Assess the morphology of the erythrocytes.
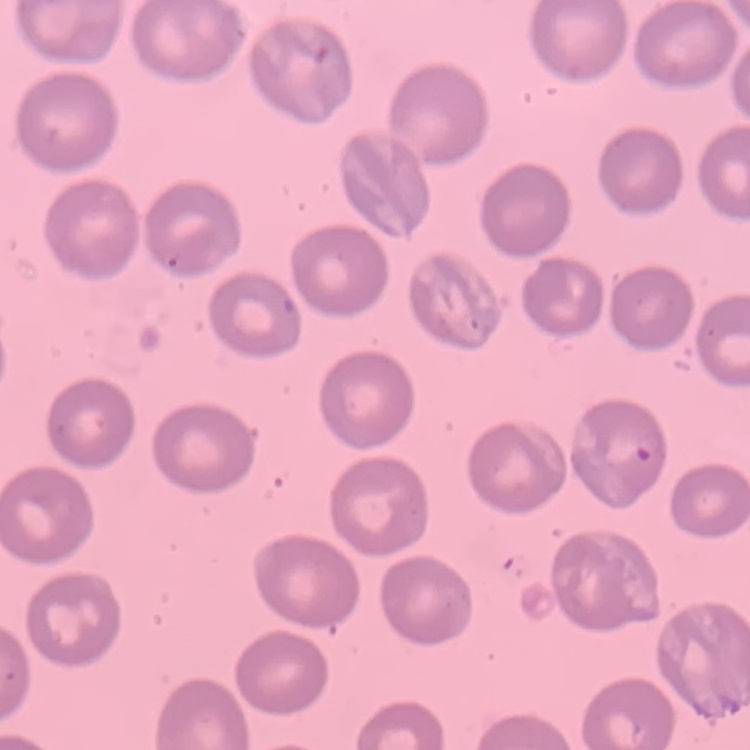
No rouleaux formation.

Summary:
  - Preparation: thin peripheral smear
  - Stain: Field's or Giemsa
  - Image type: square crop of a larger photomicrograph